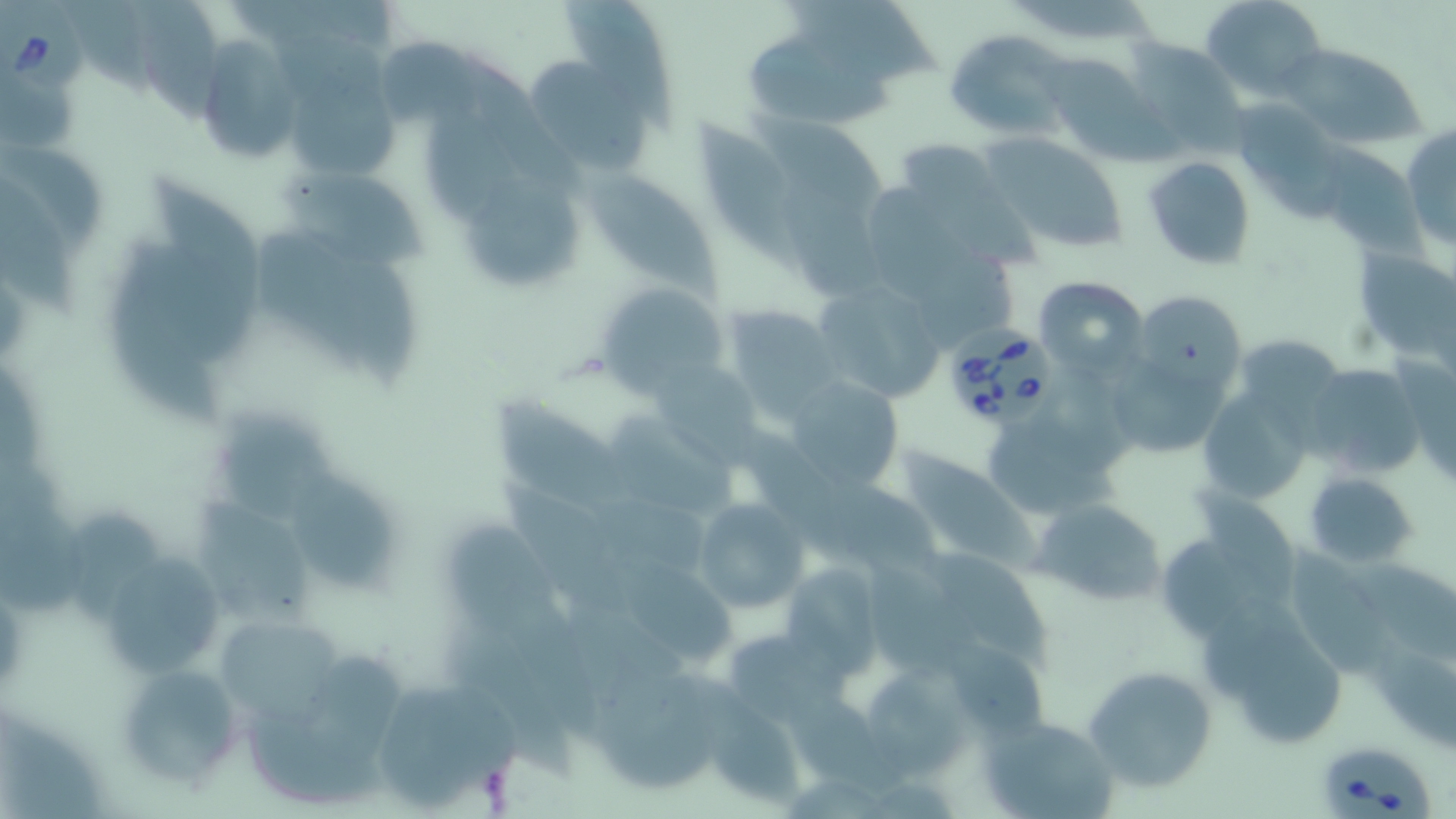
Summary:
  - Coordinate format: approximate bounding boxes as (x1, y1, x2, y2) in pixels
  - Uninfected red blood cell locations: (561, 0, 684, 136), (1200, 0, 1324, 101), (125, 1, 230, 126), (785, 2, 944, 93), (946, 29, 1075, 143), (752, 35, 902, 130), (381, 37, 493, 127), (1123, 37, 1247, 151), (191, 38, 301, 166), (1277, 41, 1429, 149), (1039, 53, 1159, 159), (529, 58, 649, 178), (1231, 101, 1346, 214), (751, 107, 888, 217), (691, 113, 805, 269), (1401, 124, 1456, 255), (980, 131, 1132, 256), (891, 138, 1011, 234), (1313, 145, 1426, 258), (1143, 156, 1256, 271), (285, 172, 435, 272), (155, 173, 267, 317), (589, 174, 719, 297), (463, 176, 588, 286), (0, 182, 88, 321), (869, 182, 1009, 312), (1352, 246, 1456, 361), (111, 265, 226, 426), (1034, 275, 1150, 376), (812, 278, 949, 405), (597, 281, 730, 399), (1134, 288, 1248, 397), (723, 304, 842, 413), (649, 359, 760, 460), (1113, 361, 1221, 450), (1304, 362, 1424, 481), (782, 376, 907, 493), (1199, 387, 1319, 508), (496, 391, 632, 511), (978, 400, 1124, 521), (612, 411, 737, 513), (215, 415, 341, 527), (892, 450, 1040, 571), (497, 472, 633, 622), (1304, 472, 1418, 567), (294, 475, 400, 592), (692, 497, 810, 615), (1033, 499, 1167, 605), (193, 501, 321, 623), (62, 504, 168, 629), (1170, 507, 1298, 634), (448, 522, 559, 634), (929, 546, 1061, 666), (102, 560, 229, 682), (780, 562, 882, 673), (1209, 606, 1352, 748), (222, 621, 345, 730), (446, 621, 576, 779), (724, 627, 836, 725), (949, 635, 1060, 738), (305, 651, 407, 756), (114, 661, 245, 792), (1084, 666, 1216, 790), (862, 667, 980, 779), (596, 669, 717, 793), (703, 702, 805, 810), (251, 708, 382, 805), (979, 715, 1114, 819)
  - Babesia divergens-infected red blood cell locations: (0, 1, 88, 102), (944, 329, 1055, 425), (1321, 745, 1435, 819)
  - Slide-level diagnosis: Babesia divergens
  - Image size: 1456×819 pixels
  - Preparation: thin blood film
  - Modality: optical microscopy
  - Field of view: one of a larger specimen
  - Stain: May-Grünwald-Giemsa
  - Magnification: 1000x